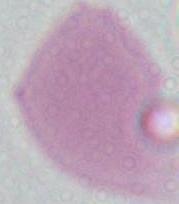
identification = erythrocyte
modality = micrograph
magnification = 1000x